Name the parasite shown.
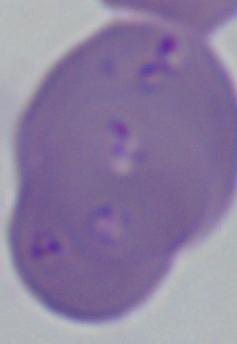
This is Babesia.

{
  "modality": "micrograph",
  "magnification": "1000x"
}